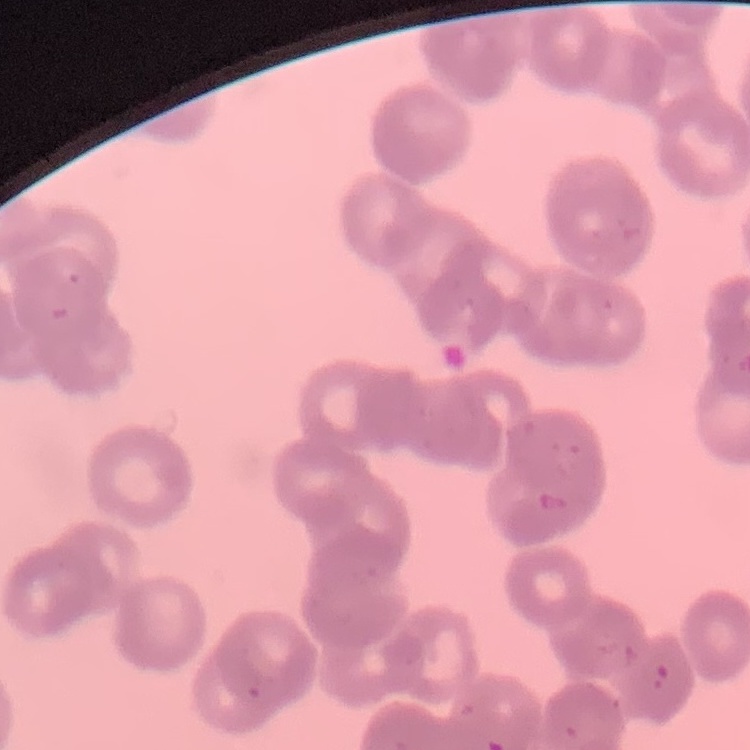

Summary:
  - Red blood cell morphology: rouleaux formation
  - Image type: square crop of a larger photomicrograph
  - Stain: Field's or Giemsa
  - Preparation: thin blood film